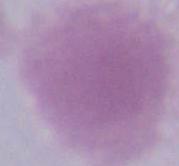
Summary:
  - Magnification: 1000x
  - Identification: erythrocyte
  - Modality: photomicrograph